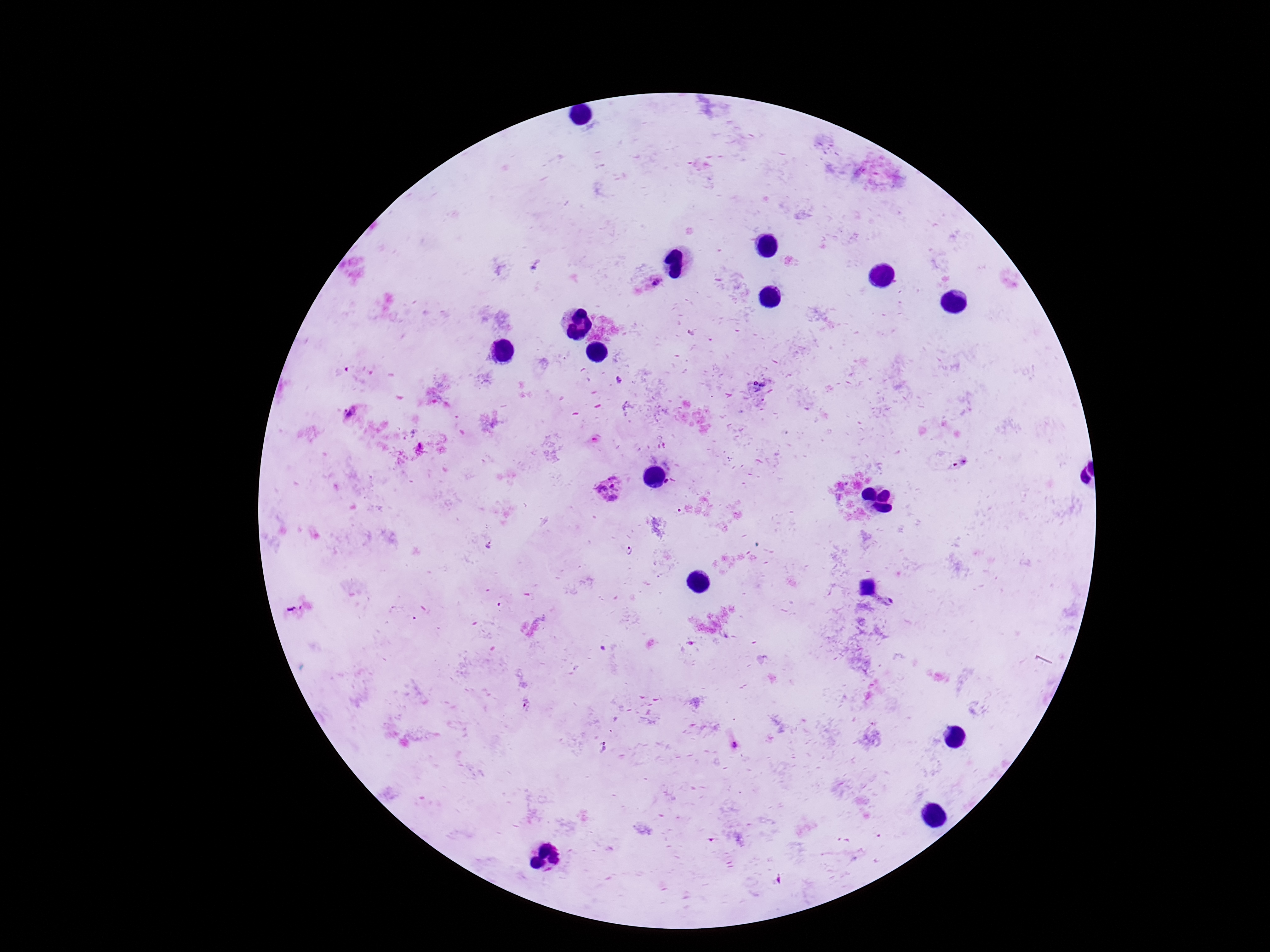

Approximate centers as (x, y) in pixels.
Summary:
  - Plasmodium parasite locations: (654, 280), (349, 415), (607, 489), (489, 545), (629, 550)
  - Magnification: 100x
  - Capture: smartphone camera through the microscope eyepiece
  - Field of view: one from this slide
  - Image size: 1270×952 pixels
  - Stain: Giemsa
  - Patient malaria status: infected
  - Preparation: thick blood smear